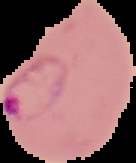
Summary:
  - Preparation: thin blood smear
  - Result: Plasmodium parasites identified
  - Image type: segmented cell region on a black background
  - Image size: 136×163 pixels